Classify this cell by malaria status.
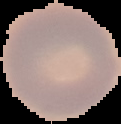

Uninfected.

image_type: segmented cell region on a black background
image_size: 121×124 pixels
preparation: thin blood smear